State which parasite is depicted.
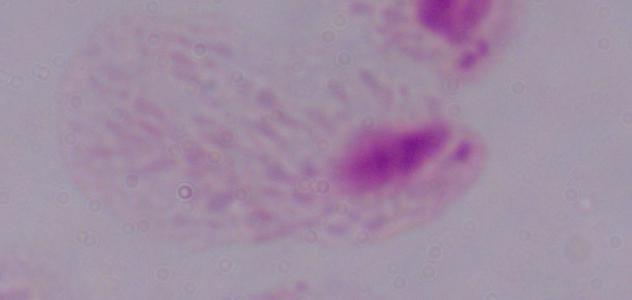

This is a trichomonad.

Summary:
  - Modality: photomicrograph
  - Magnification: 1000x